Assess this cell for malaria.
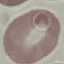

It is uninfected.

Thin blood film. Giemsa stain. Cell patch, automatically extracted from a larger field of view and resized to 64 × 64 pixels. Acquired by smartphone through the microscope eyepiece.